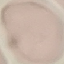
Summary:
  - Result: no malaria parasites detected
  - Capture: smartphone camera at the microscope eyepiece
  - Image type: cell patch, automatically extracted from a larger field of view and resized to 64 × 64 pixels
  - Preparation: thin blood film
  - Stain: Giemsa